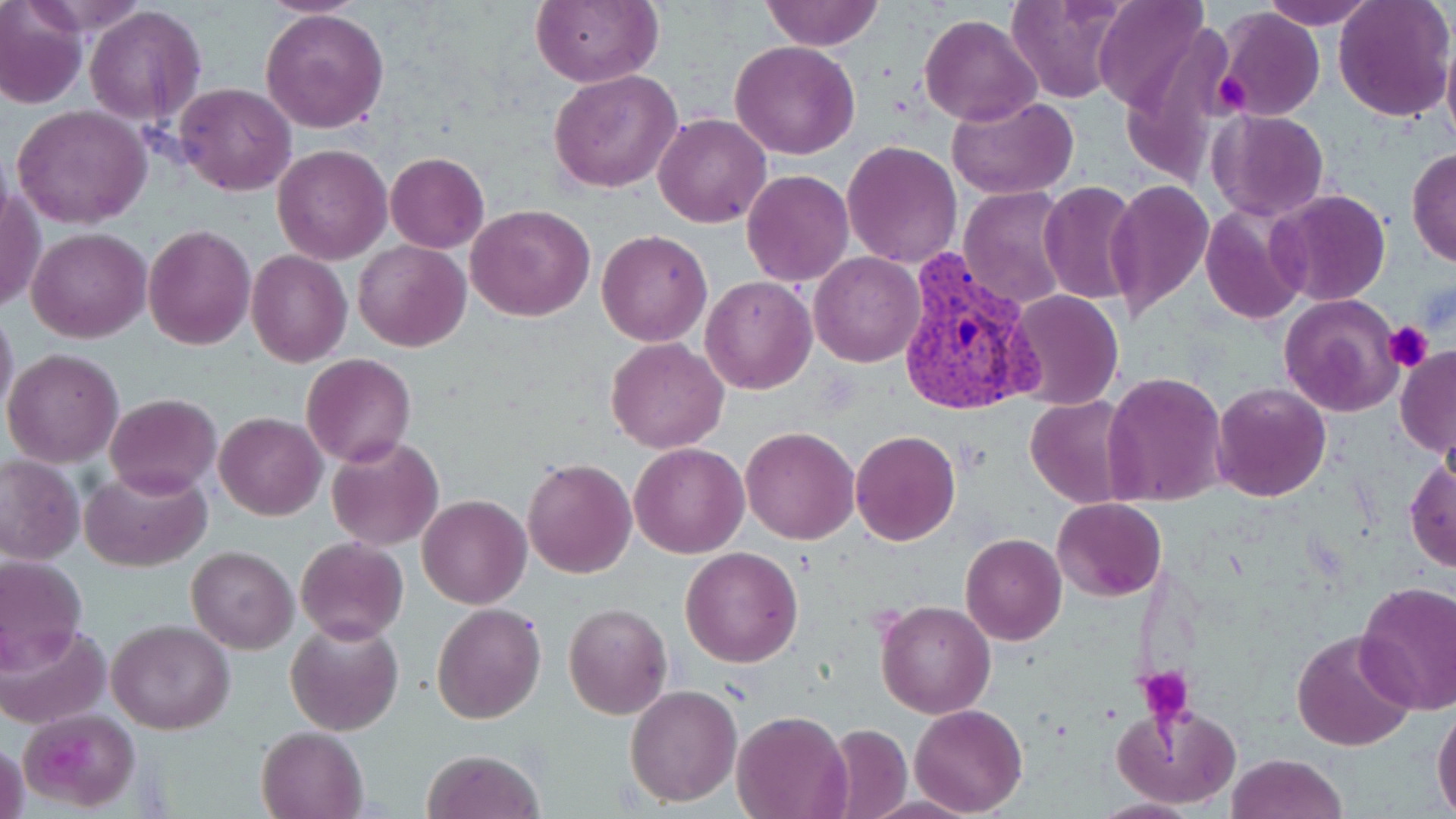

Approximate bounding boxes as named x1/y1/x2/y2 corners in pixels. Uninfected red blood cell locations: (x1=256, y1=0, x2=375, y2=17), (x1=531, y1=0, x2=659, y2=87), (x1=760, y1=0, x2=884, y2=51), (x1=1007, y1=0, x2=1129, y2=105), (x1=1261, y1=0, x2=1376, y2=29), (x1=1333, y1=0, x2=1454, y2=121), (x1=1091, y1=1, x2=1211, y2=114), (x1=0, y1=4, x2=86, y2=109), (x1=85, y1=5, x2=205, y2=125), (x1=260, y1=7, x2=389, y2=135), (x1=1214, y1=9, x2=1324, y2=121), (x1=918, y1=13, x2=1040, y2=126), (x1=1117, y1=18, x2=1236, y2=194), (x1=1440, y1=36, x2=1456, y2=159), (x1=729, y1=40, x2=861, y2=160), (x1=548, y1=69, x2=682, y2=193), (x1=174, y1=81, x2=296, y2=197), (x1=946, y1=95, x2=1080, y2=200), (x1=13, y1=105, x2=151, y2=228), (x1=1208, y1=109, x2=1330, y2=221), (x1=653, y1=112, x2=773, y2=228), (x1=843, y1=140, x2=962, y2=268), (x1=272, y1=144, x2=392, y2=265), (x1=1406, y1=148, x2=1456, y2=269), (x1=386, y1=152, x2=489, y2=254), (x1=741, y1=171, x2=854, y2=287), (x1=1104, y1=179, x2=1213, y2=320), (x1=1, y1=180, x2=43, y2=317), (x1=1038, y1=181, x2=1141, y2=306), (x1=959, y1=186, x2=1072, y2=310), (x1=1269, y1=189, x2=1391, y2=307), (x1=466, y1=204, x2=595, y2=321), (x1=1200, y1=205, x2=1309, y2=324), (x1=143, y1=224, x2=257, y2=350), (x1=26, y1=227, x2=150, y2=343), (x1=597, y1=228, x2=712, y2=346), (x1=353, y1=240, x2=470, y2=351), (x1=246, y1=250, x2=351, y2=366), (x1=810, y1=253, x2=923, y2=367), (x1=700, y1=274, x2=817, y2=394), (x1=1004, y1=290, x2=1124, y2=410), (x1=1278, y1=293, x2=1405, y2=417), (x1=0, y1=304, x2=18, y2=421), (x1=605, y1=338, x2=730, y2=453), (x1=1396, y1=345, x2=1456, y2=459), (x1=3, y1=347, x2=125, y2=467), (x1=302, y1=354, x2=415, y2=468), (x1=1102, y1=371, x2=1229, y2=506), (x1=1210, y1=381, x2=1332, y2=503), (x1=103, y1=394, x2=221, y2=497), (x1=1025, y1=395, x2=1139, y2=507), (x1=216, y1=412, x2=327, y2=520), (x1=740, y1=425, x2=860, y2=545), (x1=850, y1=430, x2=960, y2=545), (x1=327, y1=434, x2=445, y2=551), (x1=629, y1=442, x2=748, y2=558), (x1=0, y1=455, x2=85, y2=564), (x1=1404, y1=457, x2=1455, y2=572), (x1=520, y1=458, x2=636, y2=579), (x1=82, y1=465, x2=209, y2=571), (x1=417, y1=495, x2=532, y2=609), (x1=1052, y1=497, x2=1166, y2=602), (x1=961, y1=532, x2=1066, y2=645), (x1=295, y1=536, x2=409, y2=645), (x1=187, y1=545, x2=298, y2=654), (x1=680, y1=546, x2=803, y2=667), (x1=0, y1=552, x2=89, y2=672), (x1=1355, y1=581, x2=1456, y2=715), (x1=876, y1=599, x2=996, y2=719), (x1=432, y1=603, x2=546, y2=723), (x1=563, y1=603, x2=672, y2=720), (x1=285, y1=617, x2=404, y2=736), (x1=106, y1=620, x2=235, y2=734), (x1=1, y1=622, x2=109, y2=730), (x1=1291, y1=628, x2=1417, y2=752), (x1=626, y1=685, x2=740, y2=806), (x1=1432, y1=701, x2=1456, y2=817), (x1=1112, y1=703, x2=1241, y2=810), (x1=909, y1=704, x2=1028, y2=817), (x1=732, y1=710, x2=852, y2=819), (x1=22, y1=711, x2=136, y2=808), (x1=825, y1=725, x2=911, y2=815), (x1=256, y1=726, x2=367, y2=819), (x1=1, y1=738, x2=29, y2=819), (x1=423, y1=748, x2=542, y2=819), (x1=1224, y1=752, x2=1350, y2=819), (x1=1088, y1=797, x2=1199, y2=818). Plasmodium vivax-infected red blood cell locations: (x1=895, y1=247, x2=1040, y2=420). Platelet locations: (x1=1210, y1=72, x2=1251, y2=116), (x1=1384, y1=321, x2=1433, y2=372), (x1=1136, y1=667, x2=1193, y2=723). Slide-level diagnosis: Plasmodium vivax. May-Grünwald-Giemsa stain. Light microscopy. Single field of view. 1000x magnification. Image is 1456×819 pixels. Thin blood smear.